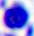
Summary:
  - Identification: leukocyte
  - Magnification: 400x
  - Modality: photomicrograph